State which parasite is depicted.
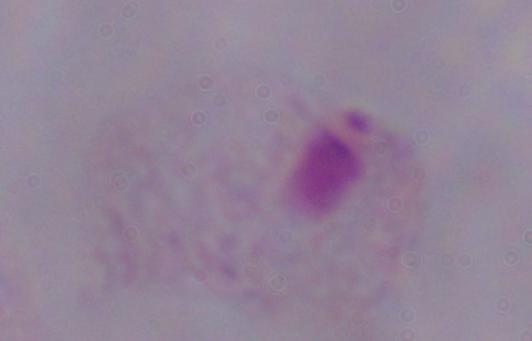

This is a trichomonad.

Summary:
  - Magnification: 1000x
  - Modality: micrograph